Locate every blood parasite and identify its species.
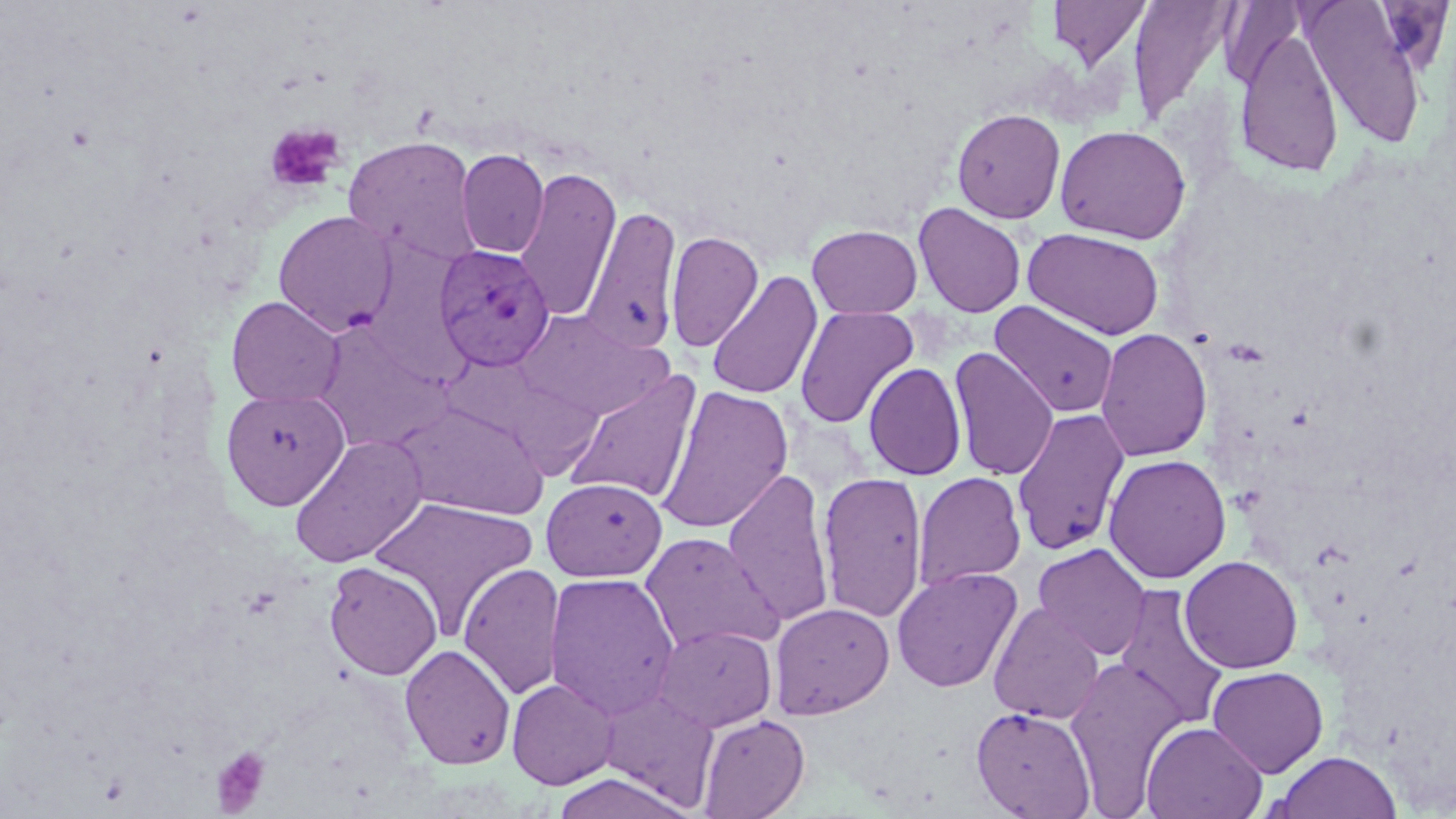

Approximate bounding boxes as (x1,y1)-(x2,y2) corner pairs in pixels.
Plasmodium vivax-infected red blood cells: (433,245)-(554,371).
No Plasmodium falciparum, Plasmodium ovale, Plasmodium malariae, Babesia divergens, or Trypanosoma brucei observed.

slide-level diagnosis = Plasmodium vivax
platelet locations = approximate bounding boxes as (x1,y1)-(x2,y2) corner pairs in pixels: (263,123)-(345,195), (210,746)-(273,815)
field of view = single
modality = optical microscopy
uninfected red blood cell locations = approximate bounding boxes as (x1,y1)-(x2,y2) corner pairs in pixels: (1047,0)-(1153,72), (1127,0)-(1237,127), (1299,0)-(1430,150), (1220,2)-(1307,89), (1233,25)-(1344,178), (951,108)-(1066,224), (1055,125)-(1191,244), (342,135)-(483,268), (456,149)-(549,258), (514,167)-(622,322), (913,202)-(1027,318), (580,206)-(683,356), (272,210)-(398,336), (807,224)-(923,319), (1022,227)-(1165,339), (365,228)-(467,383), (665,230)-(764,352), (706,270)-(822,400), (226,296)-(345,409), (989,300)-(1119,418), (794,306)-(919,428), (513,310)-(674,420), (311,324)-(453,452), (1095,327)-(1213,462), (948,346)-(1059,481), (863,361)-(967,481), (562,370)-(702,506), (655,385)-(794,534), (221,388)-(350,509), (391,401)-(549,520), (1012,408)-(1131,556), (288,433)-(429,568), (1103,453)-(1231,584), (721,467)-(835,628), (817,471)-(929,624), (913,471)-(1026,590), (541,477)-(667,582), (369,496)-(539,636), (639,532)-(784,654), (1032,542)-(1152,660), (1179,555)-(1303,674), (323,561)-(443,680), (458,562)-(567,700), (891,566)-(1023,693), (543,571)-(681,720), (1112,585)-(1230,733), (770,602)-(894,719), (987,602)-(1105,724), (653,623)-(777,732), (400,643)-(516,769), (1065,656)-(1188,813), (1207,665)-(1329,778), (506,677)-(619,789), (598,688)-(720,810), (970,706)-(1096,818), (696,713)-(810,819), (1140,720)-(1267,819), (1274,750)-(1401,819), (549,773)-(694,819)
preparation = thin blood film
magnification = 1000x
image size = 1456×819 pixels
stain = May-Grünwald-Giemsa